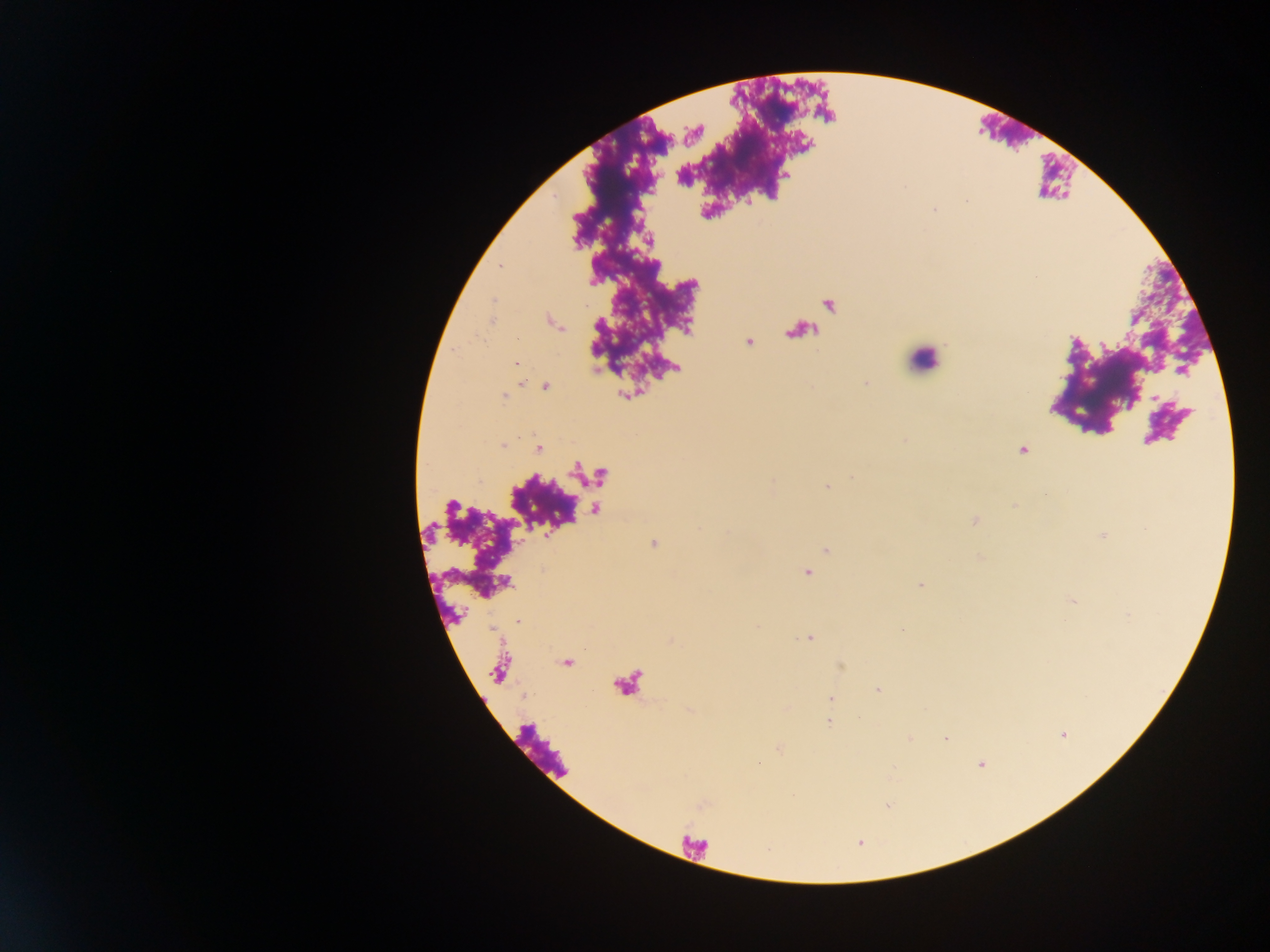

Approximate centers as x y in pixels. Malaria parasite locations: 935 211; 517 364; 545 386; 503 446; 538 449; 1022 450; 852 476; 827 486; 653 544; 826 550; 807 573; 920 585; 518 620; 810 638; 878 690; 830 698; 828 722; 946 739; 981 764. Leukocyte locations: 922 366; 540 750. Thick blood smear. Mobile-phone photograph taken through the microscope. One field of view. Collected in Ghana. Image is 1270×952 pixels.